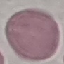
malaria status = uninfected
image type = automatically extracted cell patch, resized to 64 × 64 pixels
stain = Giemsa
preparation = thin blood film
capture = smartphone through the microscope eyepiece